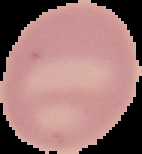
From a thin blood film. Result: no Plasmodium parasites detected. Segmented cell region on a black background. Image is 142×154 pixels.